Report the malaria status of this cell.
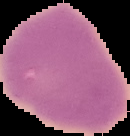

It is uninfected.

From a thin blood smear. Image is 130×136 pixels. Cell region segmented out of the field of view; the surrounding area is masked to black.